Assess the morphology of the erythrocytes.
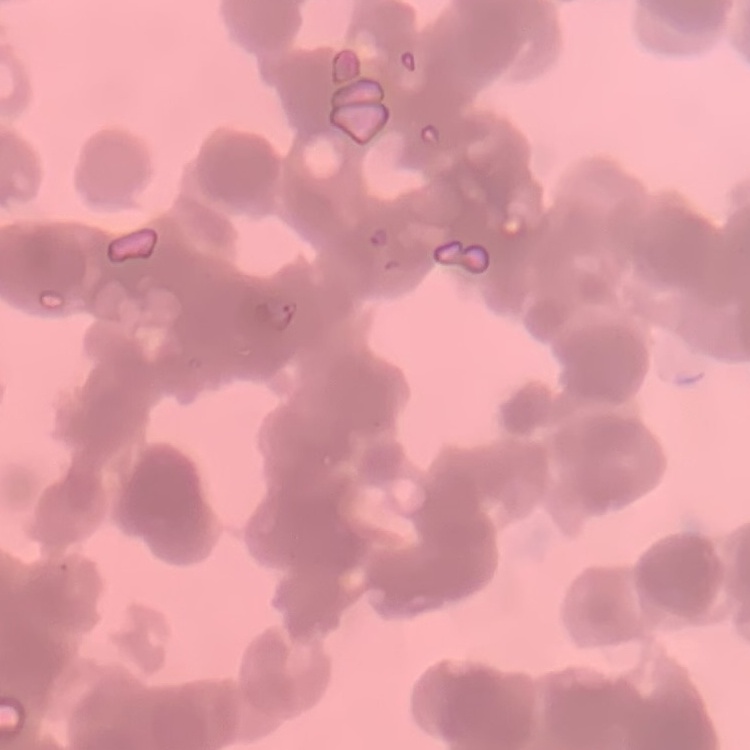
They show rouleaux formation.

Summary:
  - Preparation: thin blood smear
  - Image type: one tile cut from a larger photomicrograph
  - Stain: Field's or Giemsa